Name the cell type shown.
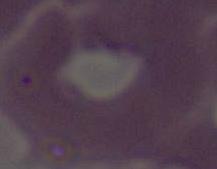

An erythrocyte.

{
  "magnification": "1000x",
  "modality": "micrograph"
}